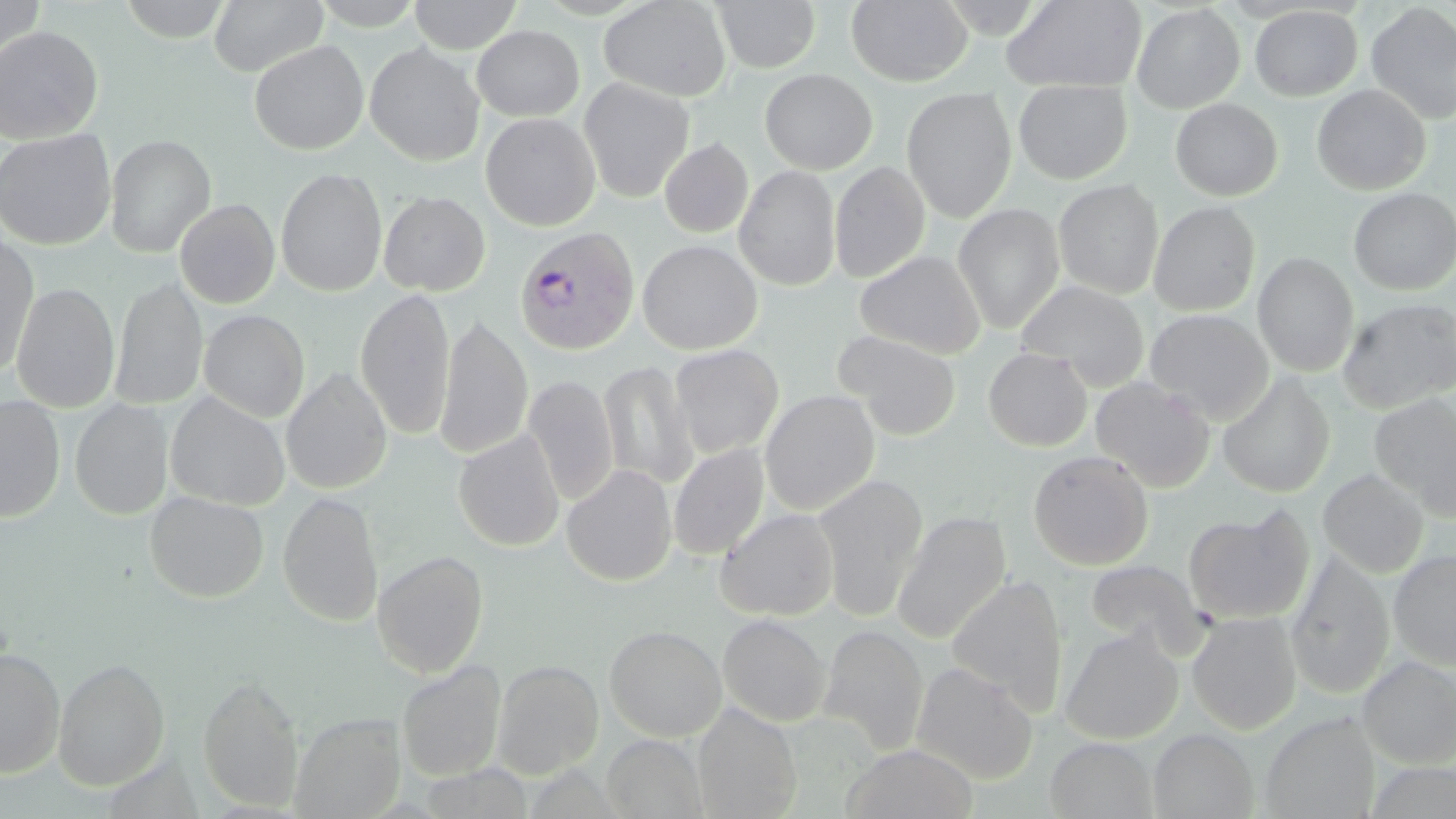
Approximate bounding boxes as (x1,y1)-(x2,y2) corner pairs in pixels. Plasmodium vivax-infected red blood cell locations: (514,226)-(639,355). Uninfected red blood cell locations: (0,0)-(46,73), (117,0)-(234,42), (208,0)-(328,77), (309,0)-(426,29), (409,0)-(523,53), (599,0)-(732,102), (714,0)-(821,72), (846,0)-(973,87), (1001,0)-(1146,93), (1366,2)-(1456,124), (1131,4)-(1245,112), (1249,5)-(1362,100), (471,24)-(584,121), (0,25)-(104,144), (249,40)-(369,155), (364,43)-(485,166), (759,69)-(877,174), (578,77)-(695,202), (1013,80)-(1132,184), (1312,84)-(1430,195), (901,87)-(1017,222), (1170,98)-(1283,200), (481,112)-(600,230), (0,128)-(116,250), (104,133)-(216,257), (660,138)-(753,237), (830,161)-(931,283), (734,164)-(841,291), (276,167)-(387,297), (1054,180)-(1163,298), (1349,188)-(1456,295), (378,190)-(491,295), (175,199)-(280,309), (1148,201)-(1260,316), (953,203)-(1064,333), (0,234)-(39,377), (637,239)-(762,355), (855,249)-(985,357), (1253,252)-(1359,376), (109,277)-(207,410), (1015,279)-(1150,388), (10,282)-(119,413), (355,288)-(456,440), (1337,297)-(1455,413), (199,309)-(310,421), (1145,309)-(1273,422), (434,316)-(532,460), (835,331)-(962,439), (670,344)-(784,458), (983,347)-(1092,451), (598,360)-(698,489), (282,367)-(392,494), (1218,373)-(1335,497), (524,374)-(619,505), (1090,376)-(1215,491), (760,389)-(880,515), (165,391)-(290,510), (1370,394)-(1456,521), (0,395)-(65,523), (70,399)-(173,519), (453,430)-(564,552), (669,443)-(769,560), (1028,450)-(1153,570), (561,464)-(677,586), (1318,468)-(1429,578), (813,473)-(927,620), (144,491)-(269,602), (277,491)-(384,627), (1183,506)-(1315,625), (716,508)-(839,620), (892,511)-(1010,643), (372,550)-(489,677), (1389,550)-(1456,669), (1286,553)-(1395,700), (1086,560)-(1207,655), (947,575)-(1068,713), (1187,612)-(1302,734), (718,614)-(832,726), (818,624)-(928,756), (605,625)-(726,741), (1059,627)-(1183,744), (0,648)-(65,778), (1357,655)-(1456,768), (53,657)-(170,790), (493,660)-(604,778), (911,661)-(1039,784), (397,662)-(505,781), (198,673)-(304,811), (692,704)-(801,819), (1260,713)-(1379,818), (291,714)-(405,818), (1148,729)-(1258,819), (601,734)-(709,819), (1045,737)-(1159,818), (841,744)-(978,819). Slide-level diagnosis: Plasmodium vivax. Thin blood film. Captured at 1000x magnification. Image is 1456×819 pixels. One field of a larger specimen. Optical microscopy. May-Grünwald-Giemsa-stained preparation.